Give the preparation type.
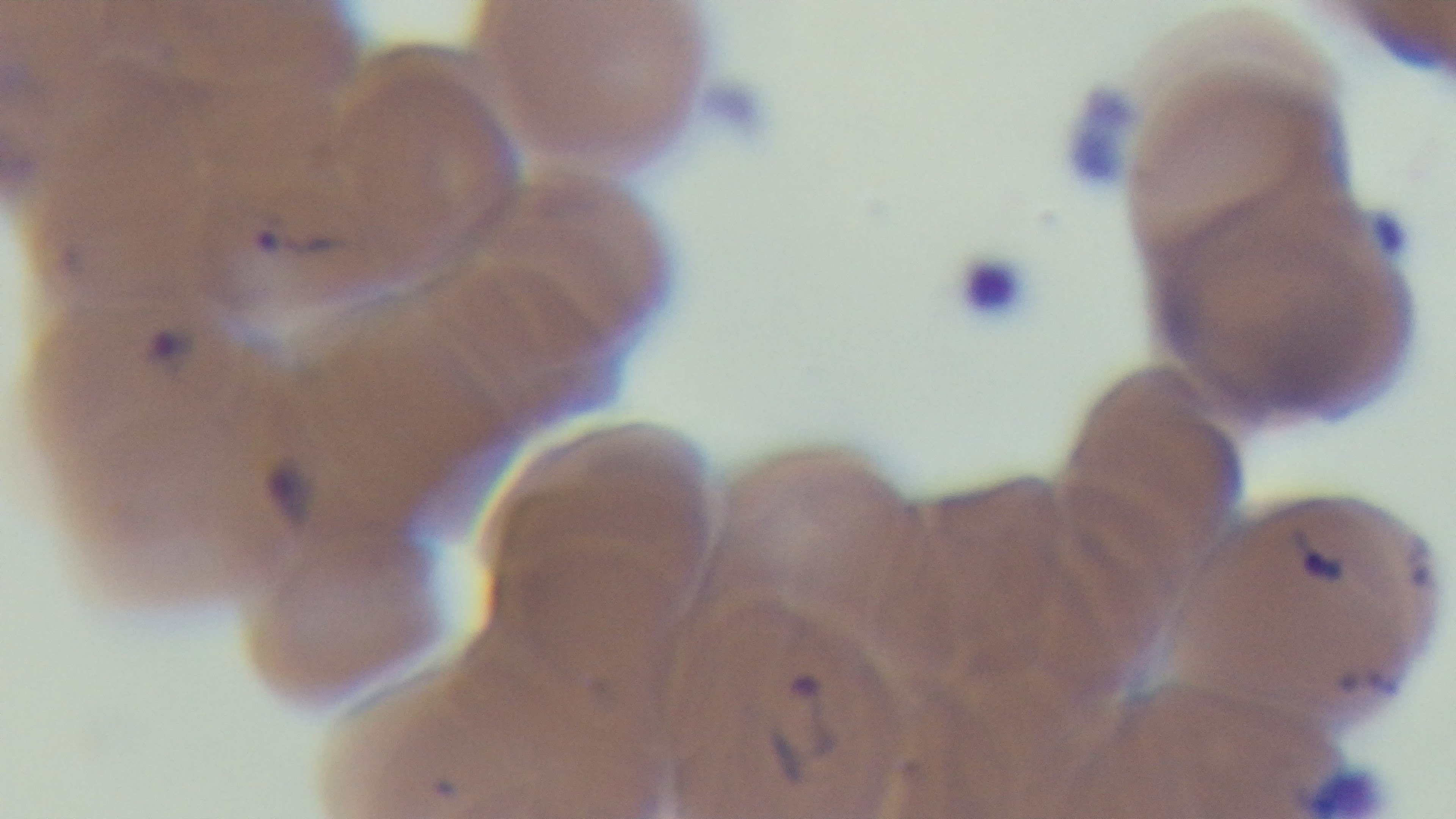
It is a thin blood film.

Summary:
  - Objective: 100x oil immersion
  - Capture: mounted 4K digital camera
  - Field of view: single
  - Stain: Giemsa
  - Modality: light microscopy
  - Malaria status: infected